Outline each uninfected red blood cell.
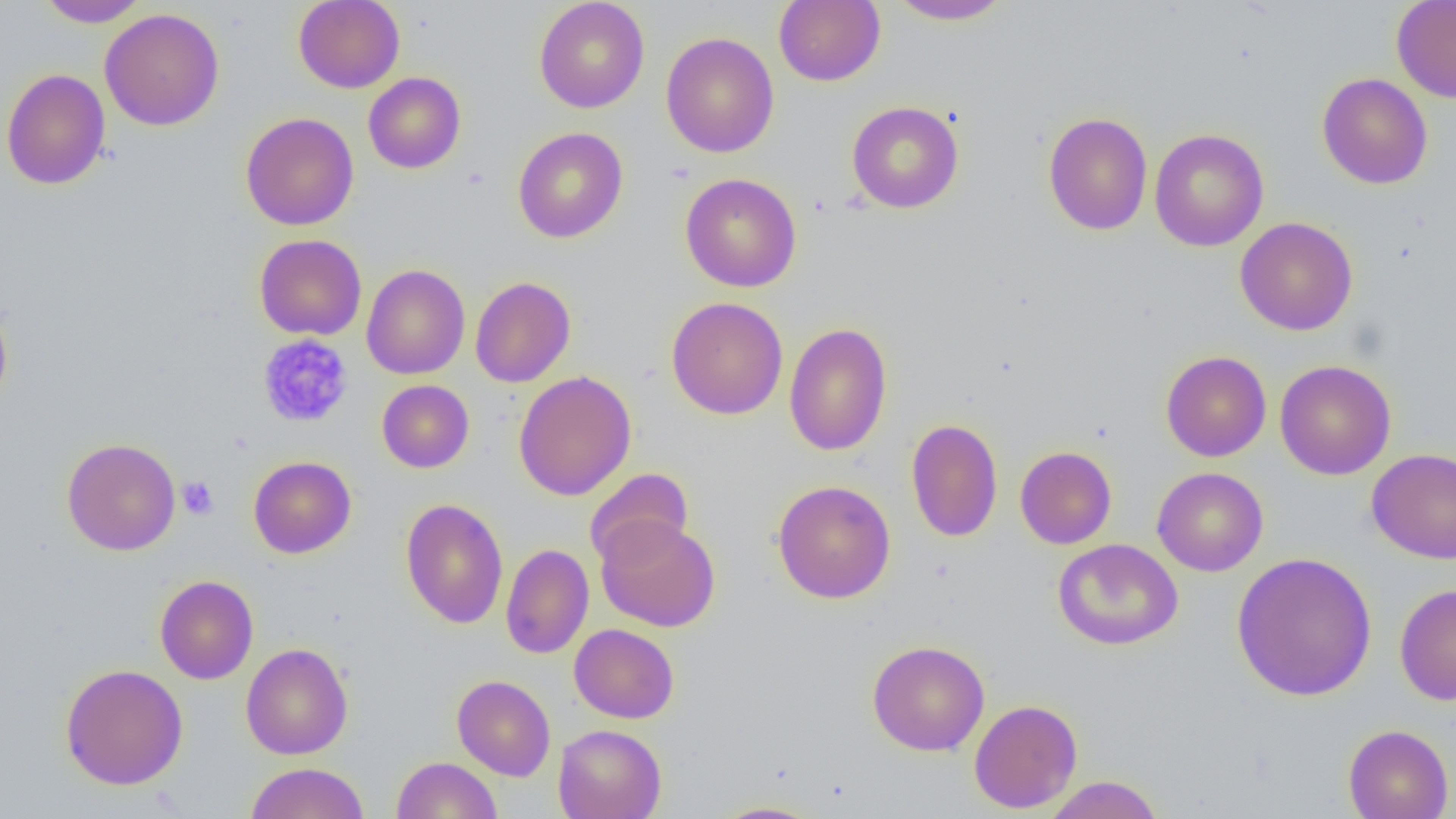

Approximate bounding boxes as (x1, y1, x2, y2) in pixels.
Uninfected red blood cells: (37, 0, 149, 27), (293, 0, 405, 93), (534, 0, 650, 113), (774, 0, 885, 86), (887, 0, 1015, 25), (1391, 0, 1456, 103), (100, 7, 225, 131), (661, 31, 779, 158), (1, 68, 111, 190), (363, 72, 466, 174), (1316, 72, 1433, 189), (847, 101, 964, 213), (240, 112, 359, 230), (1042, 112, 1153, 235), (513, 127, 628, 243), (1149, 128, 1269, 252), (680, 173, 802, 292), (1234, 216, 1358, 336), (254, 234, 367, 340), (361, 264, 470, 379), (470, 276, 576, 387), (666, 296, 788, 419), (0, 299, 13, 415), (784, 321, 893, 457), (1161, 350, 1272, 462), (1275, 359, 1396, 480), (513, 371, 637, 501), (377, 379, 475, 473), (906, 418, 1003, 542), (62, 438, 181, 556), (1015, 445, 1117, 549), (1367, 448, 1456, 564), (248, 456, 356, 558), (1152, 467, 1268, 576), (584, 468, 694, 568), (772, 480, 896, 603), (400, 498, 509, 629), (596, 515, 720, 632), (1052, 538, 1184, 650), (500, 544, 594, 659), (1231, 551, 1378, 702), (155, 575, 258, 684), (1395, 583, 1456, 705), (569, 624, 679, 723), (867, 640, 990, 756), (240, 642, 353, 759), (60, 663, 188, 790), (452, 675, 555, 781), (969, 699, 1083, 813), (553, 724, 666, 819), (1343, 724, 1453, 819), (392, 756, 502, 818), (245, 762, 369, 819), (1044, 775, 1164, 819), (710, 801, 826, 818).

{
  "slide_level_diagnosis": "negative for blood parasites",
  "image_size": "1456×819 pixels",
  "field_of_view": "single",
  "magnification": "1000x",
  "preparation": "thin blood smear",
  "modality": "optical microscopy",
  "platelet_locations": "approximate bounding boxes as (x1, y1, x2, y2) in pixels: (257, 334, 353, 428), (178, 476, 218, 519)"
}